Name the parasite shown.
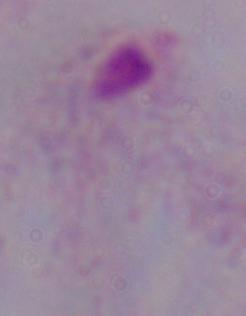

This is a trichomonad.

Captured at 1000x magnification. Photomicrograph.